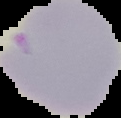

Summary:
  - Image type: segmented cell region on a black background
  - Result: negative for Plasmodium parasites
  - Preparation: thin blood smear
  - Image size: 121×118 pixels